Report the malaria status of this cell.
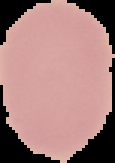
Uninfected.

image type = segmented cell region on a black background
preparation = thin blood film
image size = 115×163 pixels